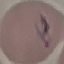

Summary:
  - Result: malaria parasites identified
  - Stain: Giemsa
  - Preparation: thin smear
  - Capture: smartphone through the microscope eyepiece
  - Image type: automatically extracted cell patch, resized to 64 × 64 pixels